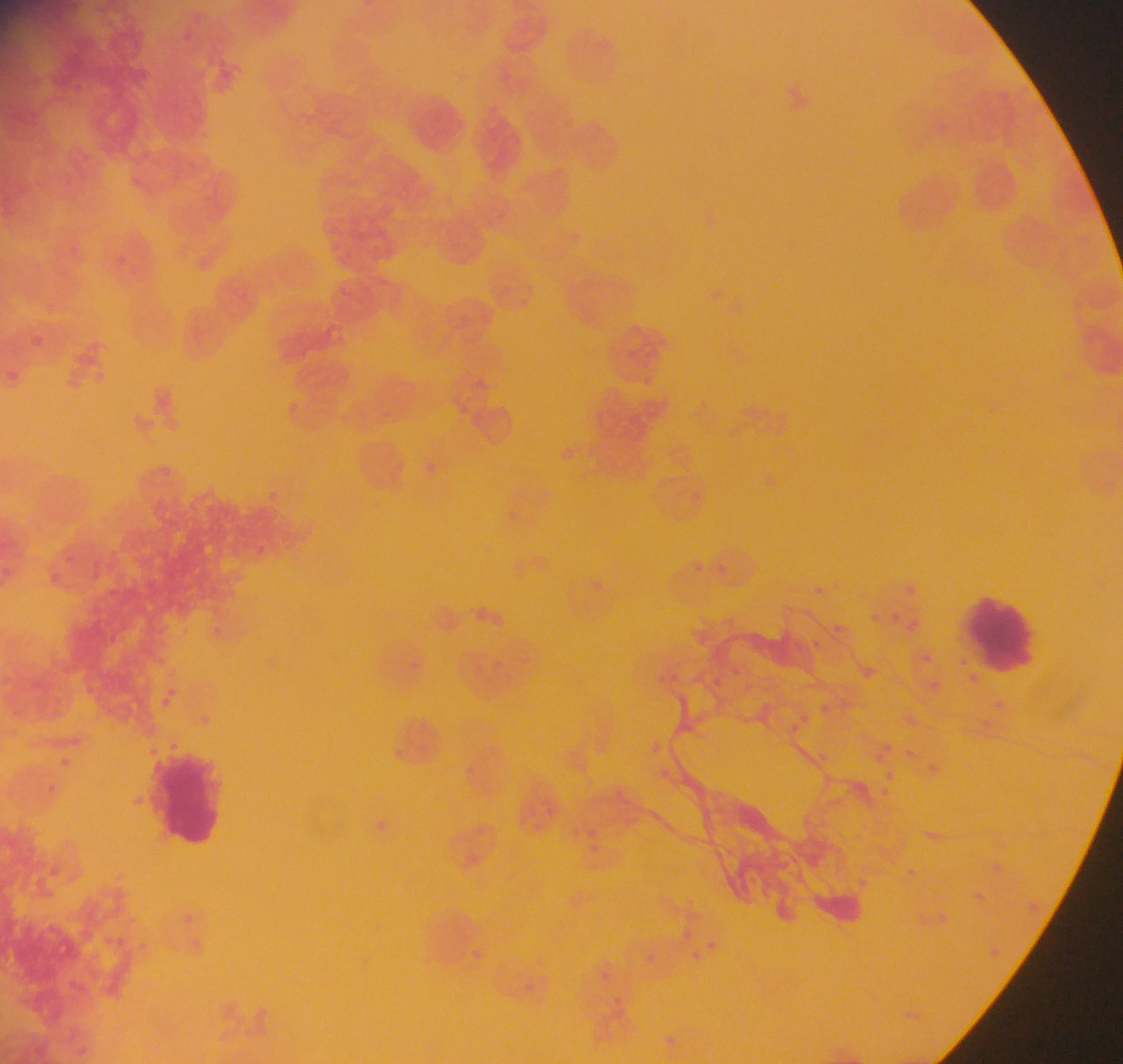
Approximate bounding boxes as left top right bottom in pixels.
Summary:
  - Plasmodium parasite locations: 116 246 129 266; 30 332 45 346; 2 363 20 379; 286 396 300 414; 567 444 580 457; 424 458 455 480; 266 487 278 493; 503 507 522 529; 257 543 282 568; 67 553 77 563; 696 556 707 568; 716 559 731 573; 52 566 68 589; 587 578 606 600; 811 582 829 594; 902 582 920 602; 864 610 886 625; 889 611 907 620; 910 617 924 627; 212 620 225 634; 832 620 845 635; 806 635 828 656; 410 648 428 678; 923 653 935 666; 863 666 878 679; 670 670 688 685; 710 672 725 687; 930 673 947 695; 165 685 184 698; 991 696 1013 712; 160 697 175 713; 817 699 837 717; 199 712 215 725; 801 712 814 724; 913 715 919 727; 978 717 996 732; 787 718 802 736; 879 737 900 755; 653 741 668 753; 906 744 915 762; 817 750 831 765; 872 754 890 769; 54 755 74 773; 461 758 479 781; 932 761 946 773; 884 772 900 787; 878 787 896 803; 520 799 536 813; 546 800 567 818; 361 813 398 844; 590 818 605 846; 584 836 609 855; 909 866 917 879; 855 874 875 895; 973 891 991 903; 1028 901 1040 913; 937 909 950 921; 680 926 695 944; 108 933 121 948; 140 936 152 951; 705 937 717 949; 990 945 1004 960; 690 947 704 966; 470 949 481 966; 641 950 663 968; 599 967 611 984; 662 1037 680 1051
  - Leukocyte locations: 405 91 473 155; 962 597 1038 674; 147 752 231 851
  - Country: Ghana
  - Preparation: thin blood film
  - Capture: mobile-phone photograph through a microscope
  - Field of view: single
  - Image size: 1123×1064 pixels